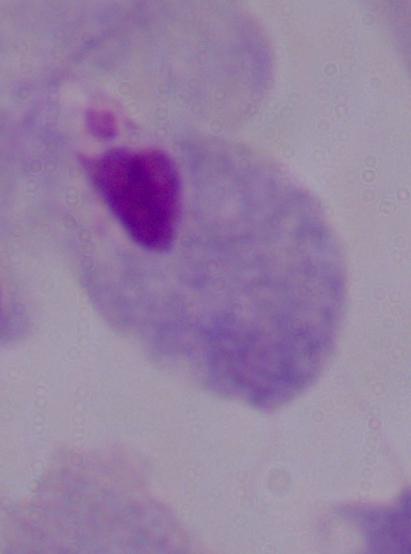

identification: trichomonad
magnification: 1000x
modality: photomicrograph